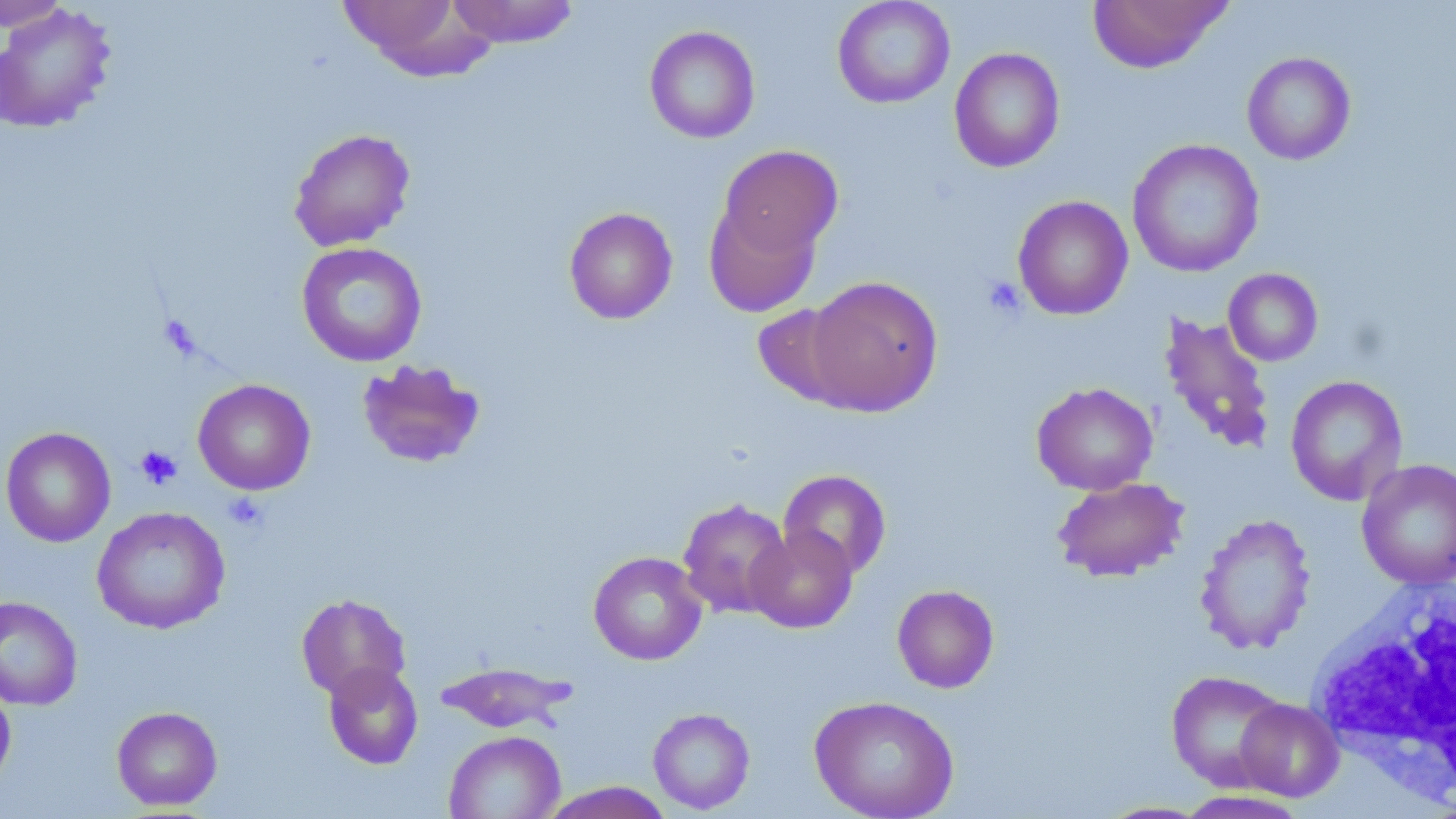

Approximate bounding boxes as named x1/y1/x2/y2 corners in pixels. Uninfected red blood cell locations: (x1=0, y1=0, x2=72, y2=33), (x1=337, y1=0, x2=492, y2=78), (x1=447, y1=0, x2=579, y2=48), (x1=832, y1=0, x2=955, y2=109), (x1=1087, y1=0, x2=1233, y2=73), (x1=0, y1=4, x2=118, y2=134), (x1=644, y1=25, x2=761, y2=144), (x1=949, y1=47, x2=1065, y2=173), (x1=1241, y1=51, x2=1356, y2=165), (x1=288, y1=128, x2=416, y2=251), (x1=1126, y1=138, x2=1265, y2=278), (x1=716, y1=145, x2=843, y2=262), (x1=1012, y1=195, x2=1133, y2=320), (x1=704, y1=202, x2=821, y2=318), (x1=563, y1=207, x2=678, y2=325), (x1=296, y1=241, x2=428, y2=367), (x1=1223, y1=268, x2=1323, y2=366), (x1=804, y1=275, x2=943, y2=416), (x1=752, y1=303, x2=862, y2=409), (x1=1158, y1=313, x2=1277, y2=457), (x1=355, y1=358, x2=487, y2=470), (x1=1285, y1=375, x2=1408, y2=507), (x1=192, y1=378, x2=316, y2=495), (x1=1031, y1=381, x2=1159, y2=495), (x1=1, y1=426, x2=116, y2=547), (x1=1356, y1=459, x2=1456, y2=590), (x1=778, y1=469, x2=892, y2=579), (x1=1051, y1=476, x2=1189, y2=583), (x1=677, y1=498, x2=794, y2=619), (x1=91, y1=506, x2=230, y2=634), (x1=1194, y1=512, x2=1316, y2=656), (x1=746, y1=526, x2=858, y2=633), (x1=588, y1=551, x2=708, y2=665), (x1=891, y1=584, x2=1000, y2=693), (x1=296, y1=592, x2=411, y2=700), (x1=0, y1=596, x2=83, y2=710), (x1=435, y1=660, x2=577, y2=735), (x1=323, y1=662, x2=423, y2=770), (x1=1167, y1=670, x2=1290, y2=791), (x1=0, y1=682, x2=16, y2=790), (x1=809, y1=694, x2=959, y2=819), (x1=1235, y1=698, x2=1344, y2=801), (x1=111, y1=706, x2=223, y2=811), (x1=647, y1=707, x2=756, y2=814), (x1=443, y1=730, x2=565, y2=818), (x1=539, y1=782, x2=674, y2=818), (x1=1173, y1=790, x2=1313, y2=819). White blood cell locations: (x1=1308, y1=573, x2=1456, y2=809). Platelet locations: (x1=981, y1=275, x2=1026, y2=320), (x1=135, y1=445, x2=183, y2=490), (x1=223, y1=492, x2=269, y2=533). Slide-level diagnosis: no evidence of blood parasites. Light microscopy. Thin blood film. Single field of view. 1000x magnification. May-Grünwald-Giemsa-stained preparation. Image is 1456×819 pixels.